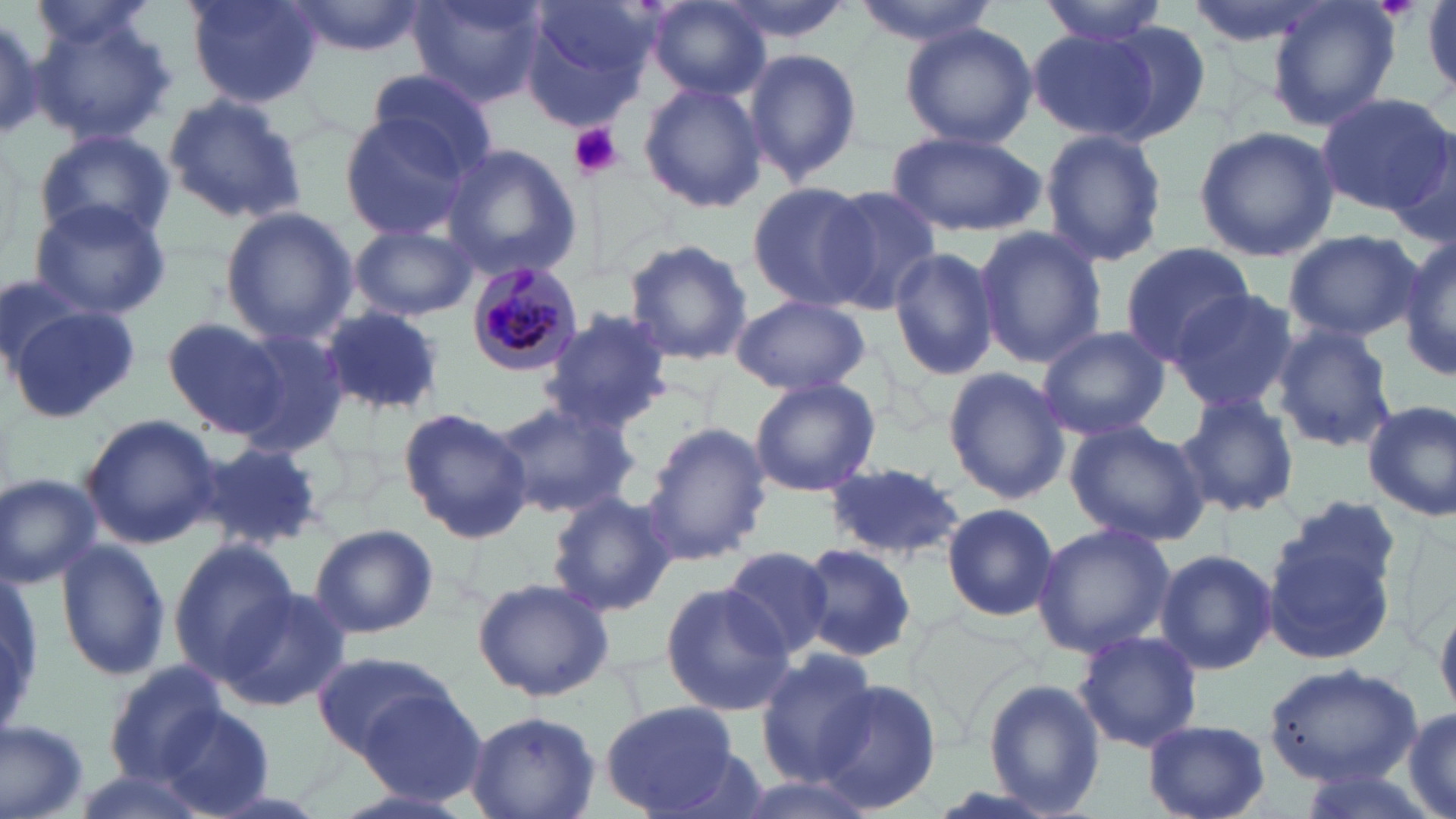
Summary:
  - Coordinate format: approximate bounding boxes as (x1,y1)-(x2,y2) corner pairs in pixels
  - Plasmodium malariae-infected red blood cell locations: (464,261)-(585,376)
  - Uninfected red blood cell locations: (183,0)-(323,106), (286,0)-(426,58), (406,0)-(549,107), (711,0)-(857,46), (851,0)-(1003,44), (1038,0)-(1171,44), (1185,0)-(1330,47), (1267,0)-(1401,132), (24,1)-(162,51), (519,1)-(657,125), (645,2)-(769,99), (0,7)-(56,142), (28,8)-(176,145), (901,23)-(1036,149), (1100,23)-(1212,141), (1024,31)-(1156,142), (742,47)-(864,188), (365,66)-(500,170), (638,82)-(770,214), (161,92)-(307,225), (1313,93)-(1453,219), (337,112)-(482,241), (1193,124)-(1337,262), (33,126)-(178,248), (882,129)-(1046,235), (1040,130)-(1167,267), (439,142)-(584,280), (750,181)-(878,312), (820,187)-(945,314), (29,197)-(173,320), (220,206)-(358,344), (348,224)-(479,322), (972,226)-(1105,367), (1283,229)-(1422,343), (1397,234)-(1456,380), (622,240)-(754,366), (1121,244)-(1260,372), (888,246)-(999,380), (1165,289)-(1299,417), (2,296)-(138,423), (729,296)-(871,395), (320,308)-(444,416), (540,308)-(675,431), (163,315)-(294,441), (1272,323)-(1397,454), (1036,325)-(1170,440), (230,327)-(353,458), (942,367)-(1071,504), (749,378)-(881,498), (1173,393)-(1300,519), (490,399)-(636,520), (1362,399)-(1456,522), (398,407)-(533,543), (82,415)-(221,547), (1063,419)-(1211,548), (640,420)-(770,567), (185,441)-(328,553), (825,463)-(968,561), (0,474)-(102,588), (547,491)-(675,619), (941,502)-(1062,622), (1263,505)-(1401,661), (308,523)-(437,640), (1031,523)-(1175,657), (55,536)-(173,681), (168,539)-(303,682), (798,544)-(917,659), (720,545)-(838,662), (1154,548)-(1277,676), (2,567)-(42,737), (472,576)-(615,702), (661,582)-(792,716), (215,588)-(352,713), (1072,630)-(1203,753), (754,648)-(880,785), (311,653)-(462,756), (103,659)-(230,784), (1262,662)-(1423,787), (819,679)-(943,812), (981,680)-(1106,815), (356,687)-(488,803), (600,699)-(746,814), (1401,704)-(1456,819), (466,707)-(600,819), (157,710)-(276,818), (1,718)-(94,818), (1142,718)-(1270,819), (1289,765)-(1442,819), (728,774)-(881,819)
  - Platelet locations: (569,121)-(622,179)
  - Slide-level diagnosis: Plasmodium malariae
  - Field of view: single
  - Preparation: thin blood film
  - Modality: optical microscopy
  - Image size: 1456×819 pixels
  - Stain: May-Grünwald-Giemsa
  - Magnification: 1000x